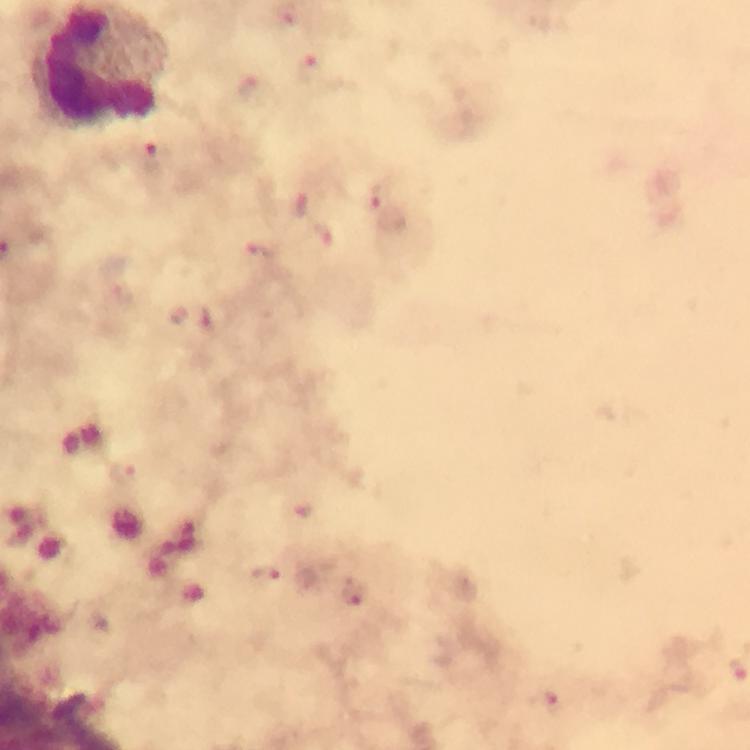
Approximate centers as [x, y] in pixels.
Summary:
  - Leukocyte locations: [109, 67]
  - Malaria parasite locations: [311, 69], [155, 161], [379, 195], [302, 205], [323, 230], [257, 251], [125, 473], [303, 512], [267, 579], [353, 591], [551, 704]
  - Cropped from: a single field of view
  - Preparation: thick blood smear
  - Magnification: 100x
  - Context: from a diagnostic examination for malaria
  - Capture: smartphone camera through the microscope
  - Image size: 750×750 pixels
  - Stain: Giemsa
  - Immersion oil: applied